Outline each uninfected red blood cell.
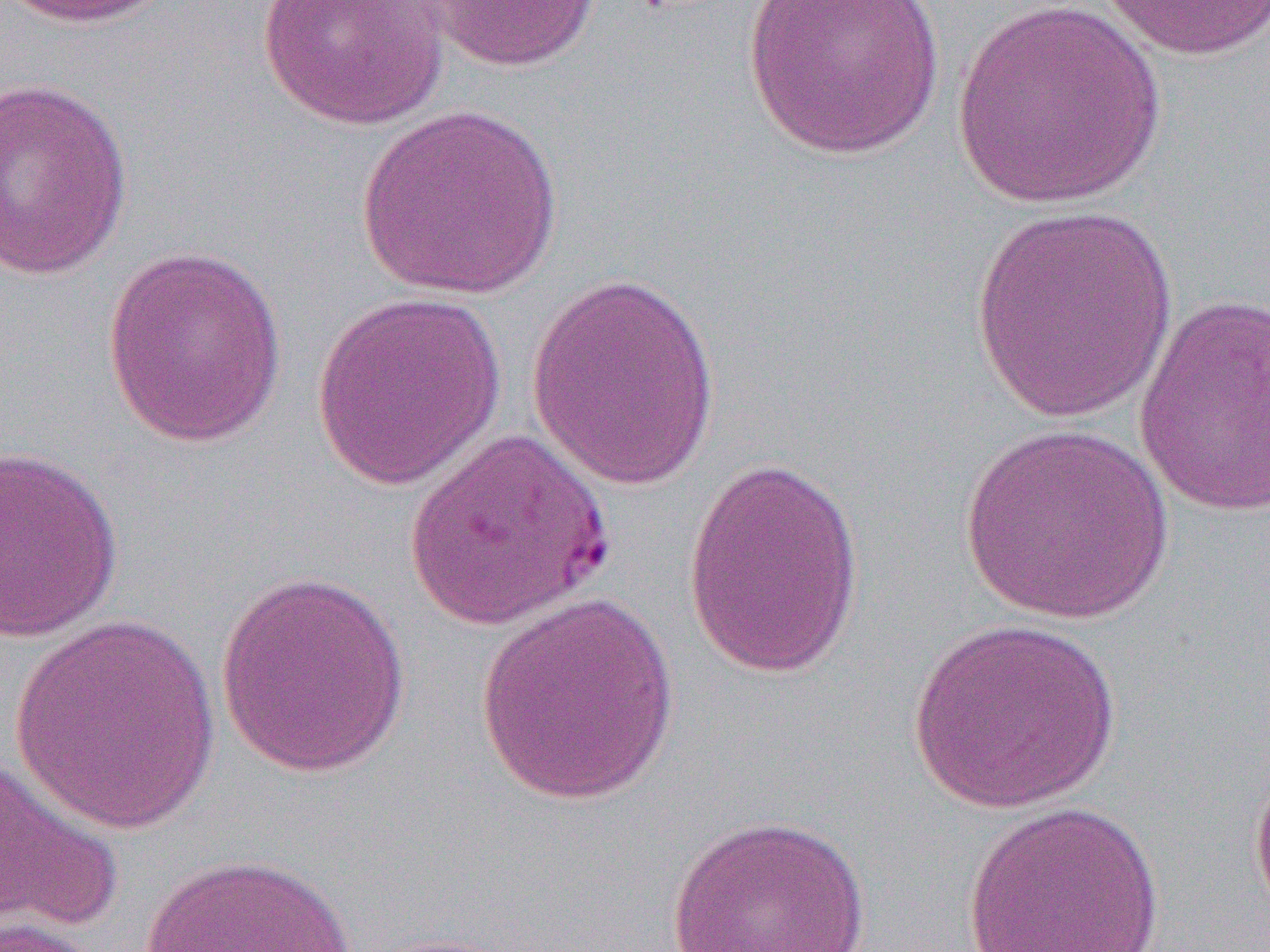
Approximate bounding boxes as (x1, y1, x2, y2) in pixels.
Uninfected red blood cells: (4, 0, 174, 29), (257, 0, 450, 131), (421, 0, 604, 72), (743, 0, 945, 161), (1092, 0, 1270, 62), (949, 2, 1168, 211), (1, 77, 135, 280), (354, 104, 565, 299), (968, 205, 1180, 424), (102, 245, 289, 448), (525, 268, 723, 495), (311, 291, 506, 491), (1133, 291, 1270, 516), (959, 422, 1173, 624), (406, 428, 614, 633), (0, 443, 125, 643), (682, 455, 866, 679), (213, 570, 412, 779), (473, 592, 682, 806), (10, 617, 223, 834), (907, 618, 1121, 814), (0, 752, 126, 939), (1250, 756, 1270, 927), (959, 799, 1168, 952), (666, 813, 873, 952), (136, 852, 366, 952), (0, 916, 101, 952).

Summary:
  - Slide-level diagnosis: Plasmodium falciparum
  - Image size: 1270×952 pixels
  - Preparation: thin blood smear
  - Magnification: 1000x
  - Field of view: single
  - Modality: light microscopy